Assess this cell for malaria.
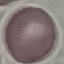

It is uninfected.

capture = smartphone camera at the microscope eyepiece
stain = Giemsa
image type = automatically extracted cell patch, resized to 64 × 64 pixels
preparation = thin smear